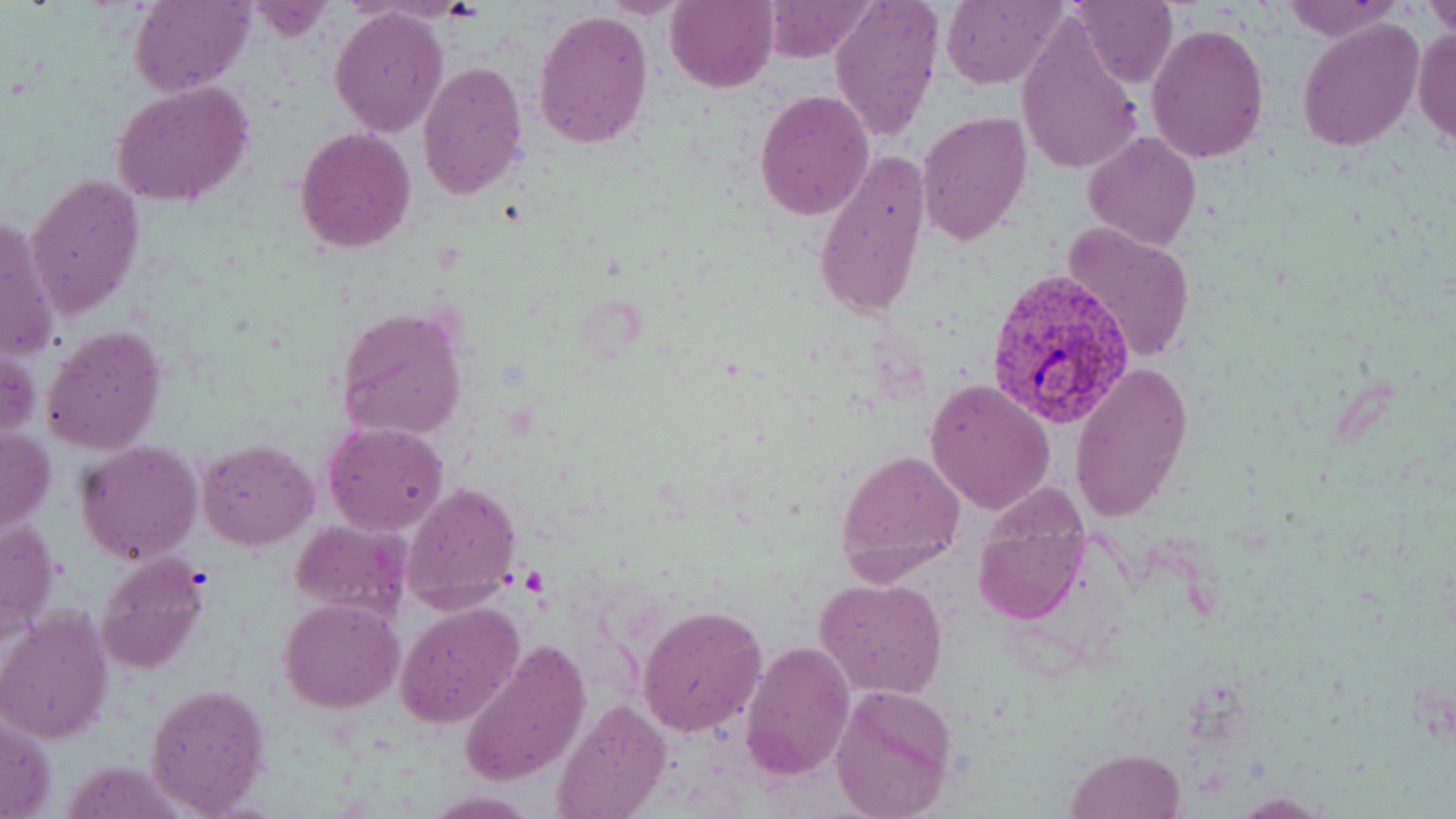 Approximate bounding boxes as (x1,y1)-(x2,y2) corner pairs in pixels. Uninfected red blood cell locations: (130,0)-(253,96), (594,0)-(690,17), (666,0)-(778,93), (766,0)-(874,60), (829,0)-(941,143), (939,0)-(1064,89), (1068,0)-(1178,88), (1279,0)-(1400,40), (1423,4)-(1456,34), (329,7)-(450,137), (533,8)-(655,150), (1016,15)-(1143,179), (1297,17)-(1424,153), (1146,22)-(1269,161), (1412,29)-(1456,150), (417,59)-(528,199), (111,82)-(255,209), (752,89)-(875,222), (917,110)-(1032,244), (295,127)-(417,253), (1082,131)-(1202,250), (813,150)-(928,324), (25,173)-(145,321), (1,215)-(58,365), (1063,223)-(1198,362), (335,307)-(468,441), (41,326)-(167,455), (1,339)-(40,450), (1068,360)-(1194,522), (925,378)-(1057,516), (321,421)-(449,535), (1,428)-(58,536), (76,440)-(203,565), (198,440)-(317,550), (836,447)-(966,576), (402,480)-(522,610), (973,507)-(1089,626), (0,511)-(61,649), (291,519)-(413,622), (97,554)-(211,675), (815,577)-(948,698), (280,598)-(402,713), (395,601)-(525,730), (637,604)-(767,737), (2,610)-(115,745), (457,639)-(592,786), (738,639)-(854,780), (143,682)-(271,815), (830,686)-(957,819), (552,699)-(672,819), (1,711)-(55,818), (1065,748)-(1184,819), (423,792)-(538,817), (1230,793)-(1332,817). Plasmodium vivax-infected red blood cell locations: (986,266)-(1136,430). Slide-level diagnosis: Plasmodium vivax. Light microscopy. 1000x magnification. One field of a larger specimen. Image is 1456×819 pixels. Thin blood film. May-Grünwald-Giemsa stain.